Assess the morphology of the erythrocytes.
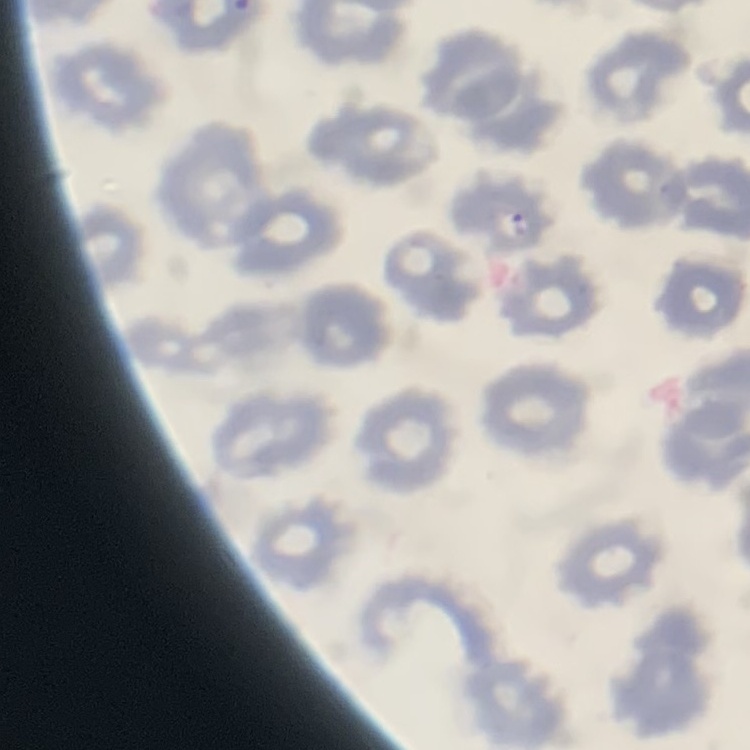
No rouleaux formation.

image type = one tile cut from a larger photomicrograph
stain = Field's or Giemsa
preparation = thin blood smear